Give the position of every leukocyte visible.
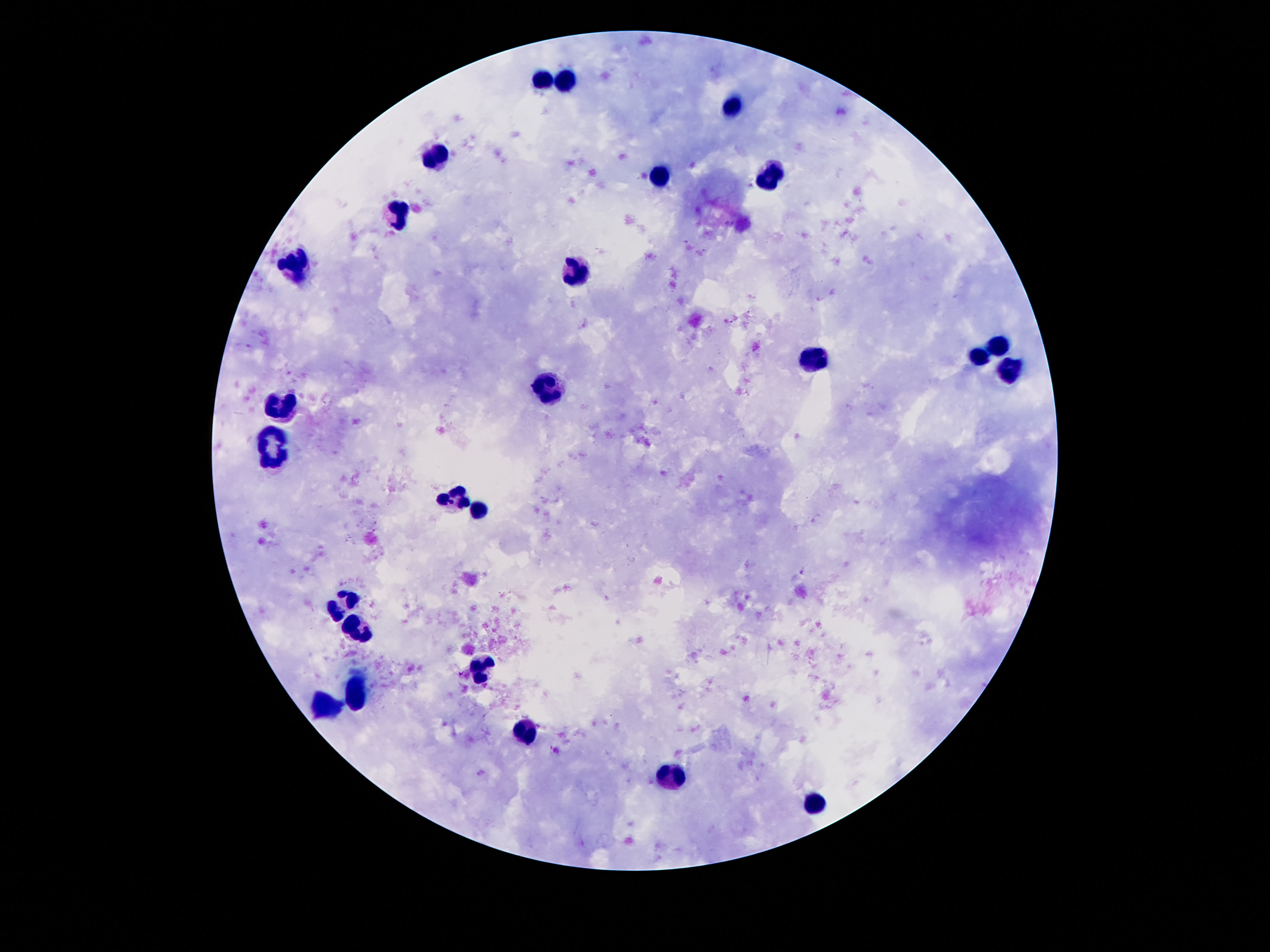
Approximate centers as (x, y) in pixels.
Leukocytes: (541, 78), (568, 79), (732, 107), (433, 155), (659, 176), (774, 176), (396, 216), (295, 268), (575, 274), (996, 347), (977, 358), (813, 361), (1012, 370), (552, 384), (281, 407), (270, 436), (275, 463), (455, 496), (477, 511), (341, 602), (357, 625), (481, 667), (357, 694), (327, 705), (526, 733), (670, 777), (814, 804).

Giemsa stain. Patient malaria status: uninfected. 100x magnification. Image is 1270×952 pixels. One field from this slide. Thick peripheral-blood smear. Smartphone photograph taken through the microscope eyepiece.